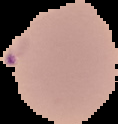

image size = 118×124 pixels
malaria status = parasitized
image type = segmented cell region on a black background
preparation = thin blood film